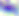
Summary:
  - Magnification: 400x
  - Modality: micrograph
  - Identification: Toxoplasma gondii